Assess the morphology of the red blood cells.
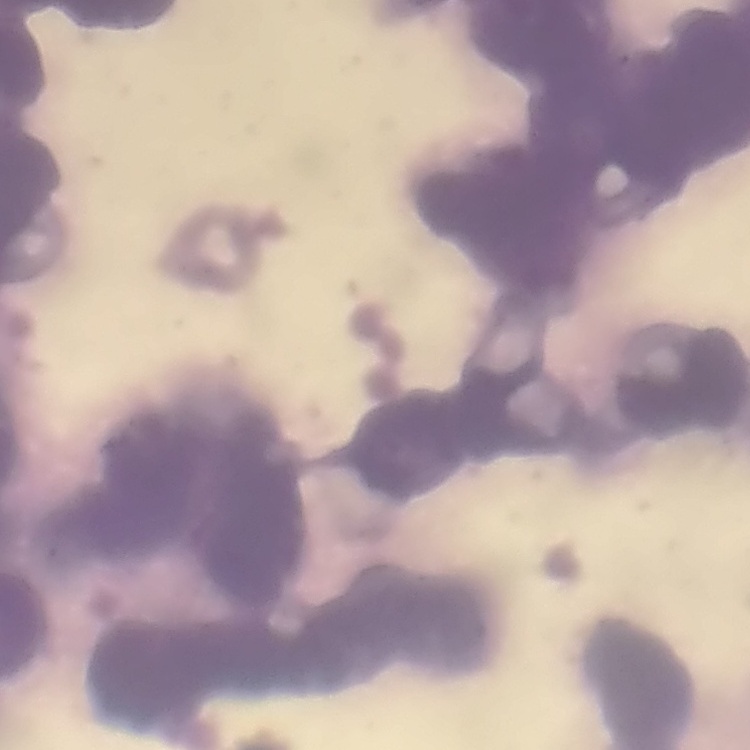
Rouleaux formation.

stain = Field's or Giemsa
image type = square crop of a larger photomicrograph
preparation = thin blood film